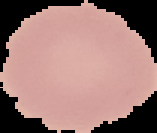
Summary:
  - Image type: segmented cell region with the area outside set to black
  - Result: negative for malaria parasites
  - Image size: 157×133 pixels
  - Preparation: thin blood film